Name the parasite shown.
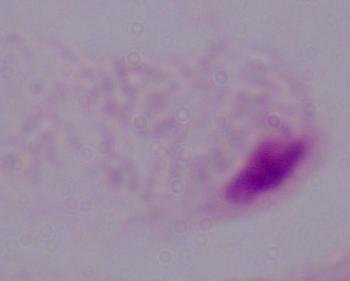

This is a trichomonad.

Photomicrograph. Captured at 1000x magnification.